Give the position of every Plasmodium parasite visible.
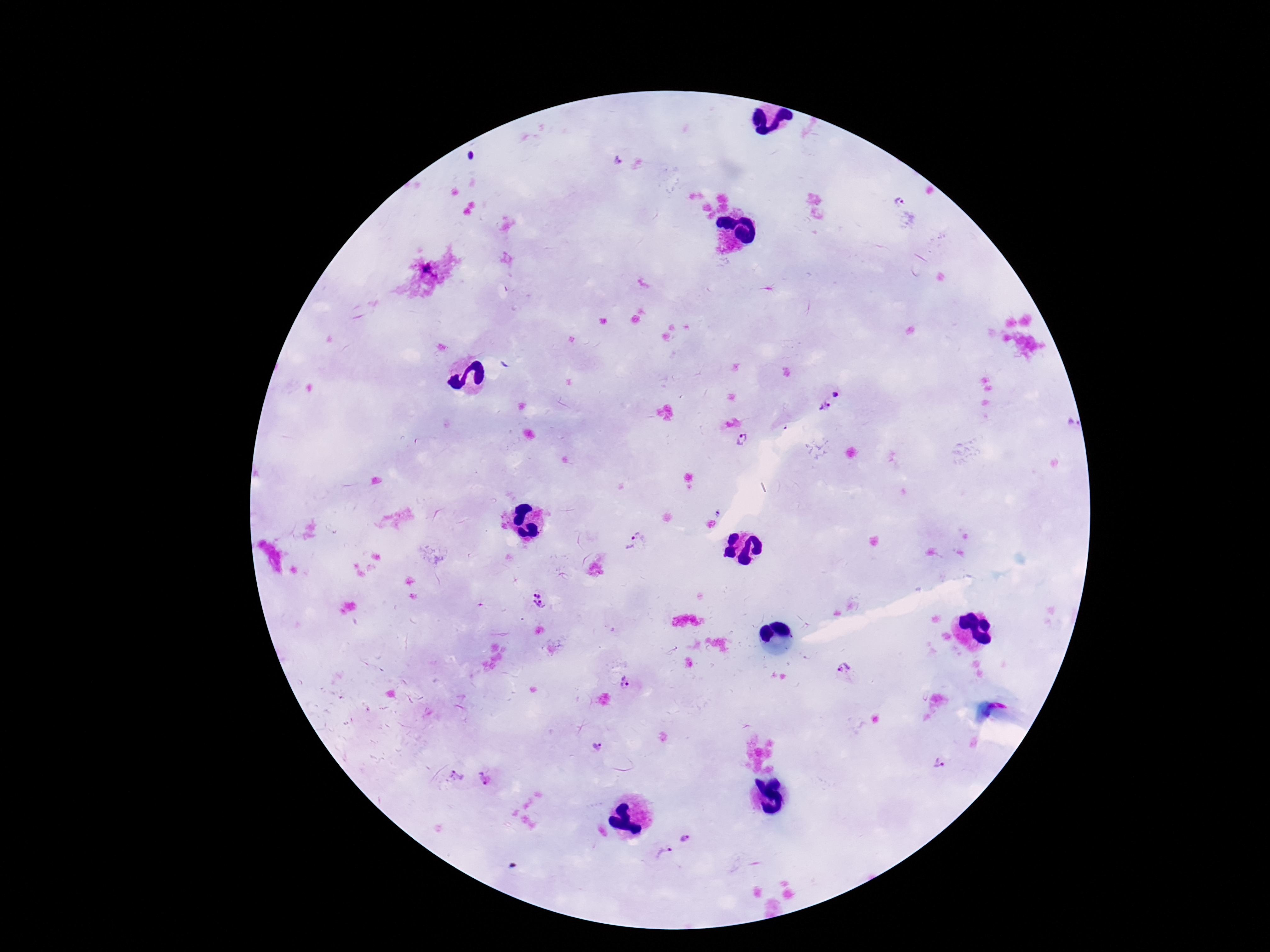

Approximate object centers, in pixels from the top-left corner.
Plasmodium parasites: (x=618, y=162), (x=901, y=202), (x=836, y=395), (x=825, y=407), (x=1072, y=424), (x=742, y=440), (x=637, y=542), (x=539, y=601), (x=843, y=670), (x=625, y=683), (x=598, y=746), (x=939, y=763), (x=456, y=775), (x=686, y=837), (x=664, y=854).

magnification = 100x
stain = Giemsa
patient malaria status = infected
image size = 1270×952 pixels
preparation = thick peripheral-blood smear
capture = smartphone camera through the microscope eyepiece
field of view = one from this slide